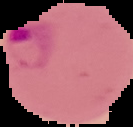
Result: Plasmodium parasites detected. Image is 133×127 pixels. The area outside the segmented cell region is set to black. From a thin blood film.